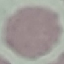
Summary:
  - Result: no malaria parasites seen
  - Preparation: thin blood smear
  - Stain: Giemsa
  - Capture: smartphone through the microscope eyepiece
  - Image type: cell patch, automatically extracted from a larger field of view and resized to 64 × 64 pixels